Give the position of every Plasmodium parasite visible.
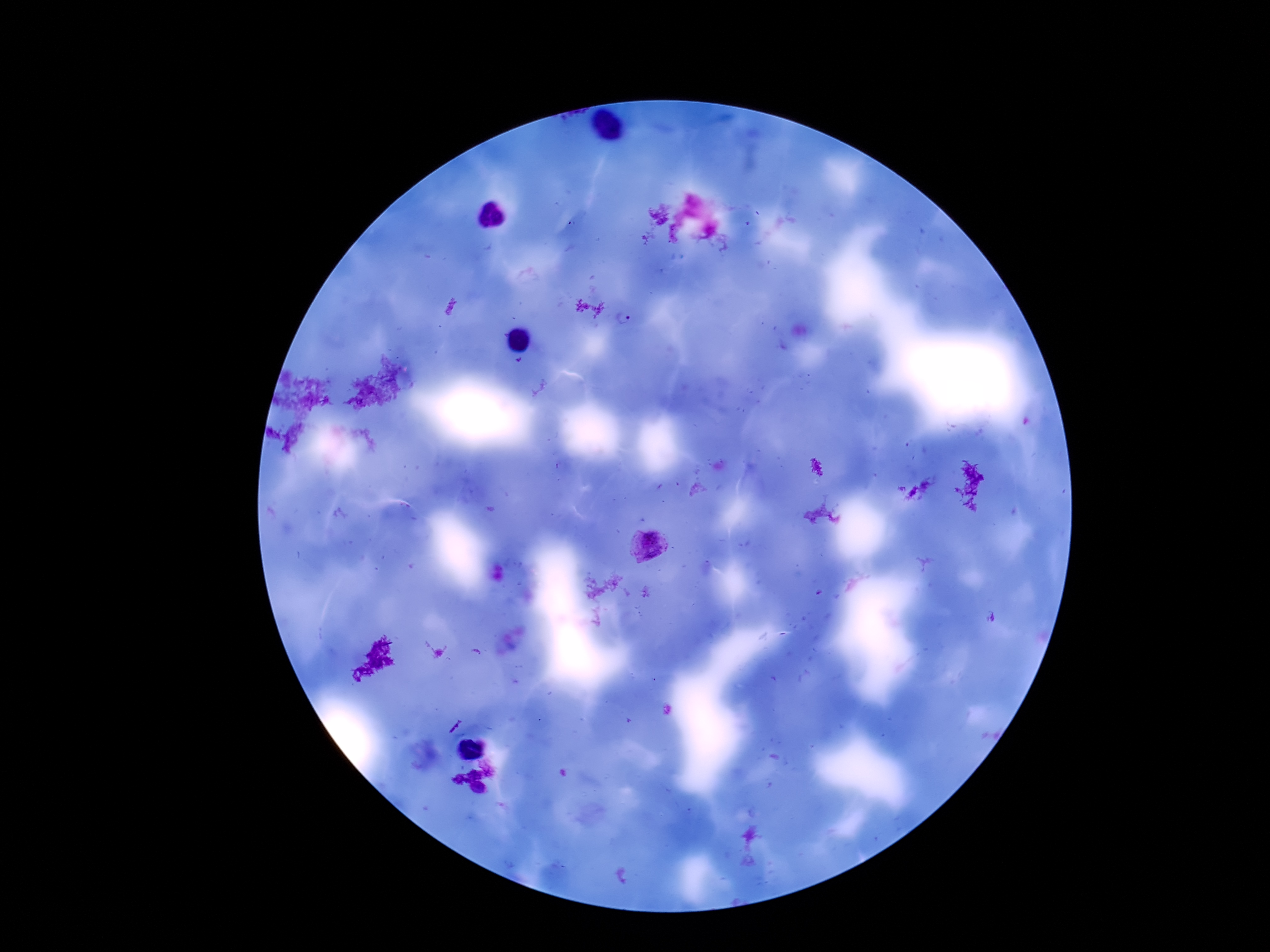

Approximate centers as (x, y) in pixels.
Plasmodium parasites: (624, 319), (647, 543).

capture: smartphone camera through the microscope eyepiece
stain: Giemsa
image_size: 1270×952 pixels
patient_malaria_status: infected
preparation: thick peripheral-blood smear
magnification: 100x
field_of_view: single